Identify the blood parasite species.
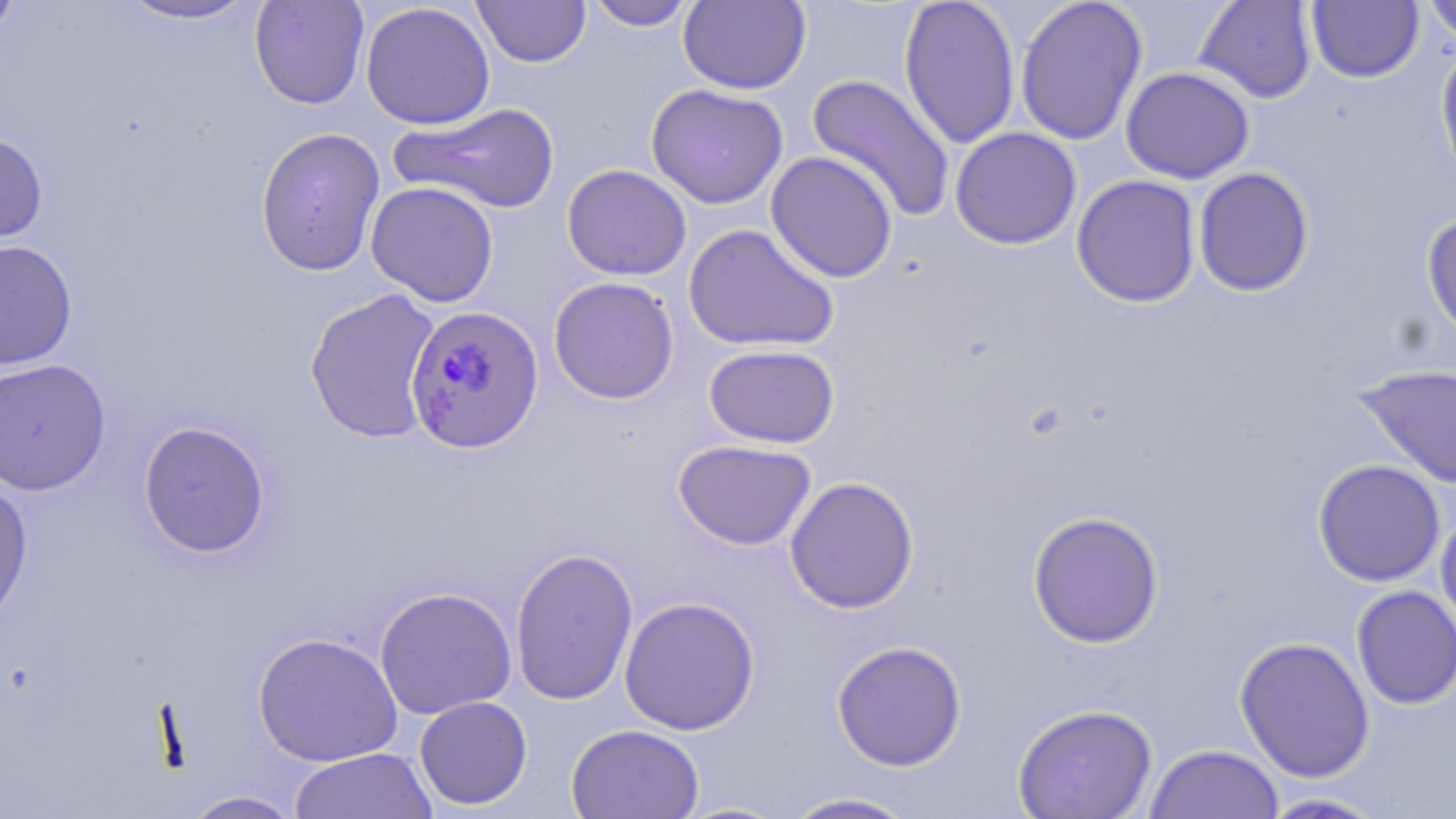

Plasmodium falciparum.

image size = 1456×819 pixels
magnification = 1000x
uninfected red blood cell locations = approximate bounding boxes as (x1, y1, x2, y2) in pixels: (112, 0, 263, 25), (249, 0, 370, 110), (472, 0, 591, 68), (584, 0, 698, 31), (898, 0, 1021, 149), (1015, 0, 1148, 146), (1194, 0, 1318, 104), (1420, 0, 1456, 46), (0, 1, 21, 45), (360, 1, 495, 130), (678, 1, 811, 94), (1306, 1, 1424, 84), (1434, 41, 1456, 190), (1121, 66, 1255, 183), (805, 73, 956, 223), (646, 84, 788, 209), (391, 102, 561, 214), (255, 127, 386, 277), (950, 127, 1082, 250), (0, 131, 49, 249), (766, 151, 899, 283), (562, 164, 692, 281), (1192, 166, 1314, 297), (1071, 174, 1201, 307), (366, 181, 499, 306), (1421, 213, 1456, 346), (683, 223, 840, 352), (0, 239, 78, 370), (549, 277, 679, 404), (305, 288, 442, 444), (704, 344, 840, 448), (0, 358, 112, 495), (1354, 363, 1455, 489), (137, 420, 272, 558), (673, 439, 816, 551), (1312, 459, 1446, 587), (0, 476, 34, 628), (784, 476, 919, 614), (1435, 508, 1456, 639), (1027, 510, 1165, 648), (509, 546, 639, 706), (1350, 585, 1456, 710), (374, 587, 517, 719), (619, 596, 760, 736), (253, 632, 404, 767), (1234, 636, 1375, 782), (832, 641, 967, 771), (414, 695, 532, 810), (1012, 703, 1158, 819), (566, 724, 704, 819), (1144, 743, 1285, 819), (288, 747, 437, 819), (181, 790, 304, 818), (779, 791, 923, 818), (1255, 791, 1391, 818)
stain = May-Grünwald-Giemsa
modality = optical microscopy
Plasmodium falciparum-infected red blood cell locations = approximate bounding boxes as (x1, y1, x2, y2) in pixels: (405, 303, 546, 455)
preparation = thin blood film
field of view = single